State which parasite is depicted.
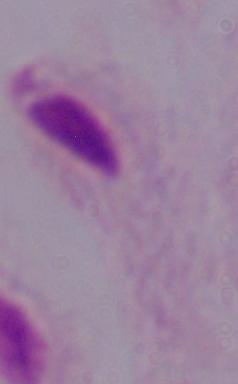
A trichomonad.

modality = photomicrograph
magnification = 1000x